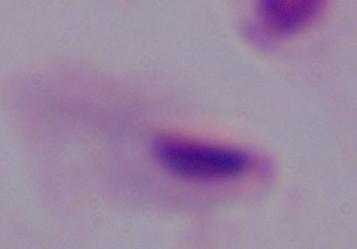

Summary:
  - Modality: photomicrograph
  - Magnification: 1000x
  - Identification: trichomonad